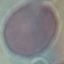
Malaria status: uninfected. Acquired by smartphone through the microscope eyepiece. Giemsa-stained preparation. Cell patch, automatically extracted from a larger field of view and resized to 64 × 64 pixels. Thin blood film.